State which cell type is depicted.
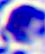

A leukocyte.

Summary:
  - Magnification: 400x
  - Modality: micrograph